Classify this cell by malaria status.
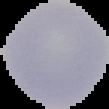
Uninfected.

image type = cell region segmented out of the field of view; surrounding area masked to black
preparation = thin blood smear
image size = 109×109 pixels